Locate every Plasmodium falciparum-infected red blood cell.
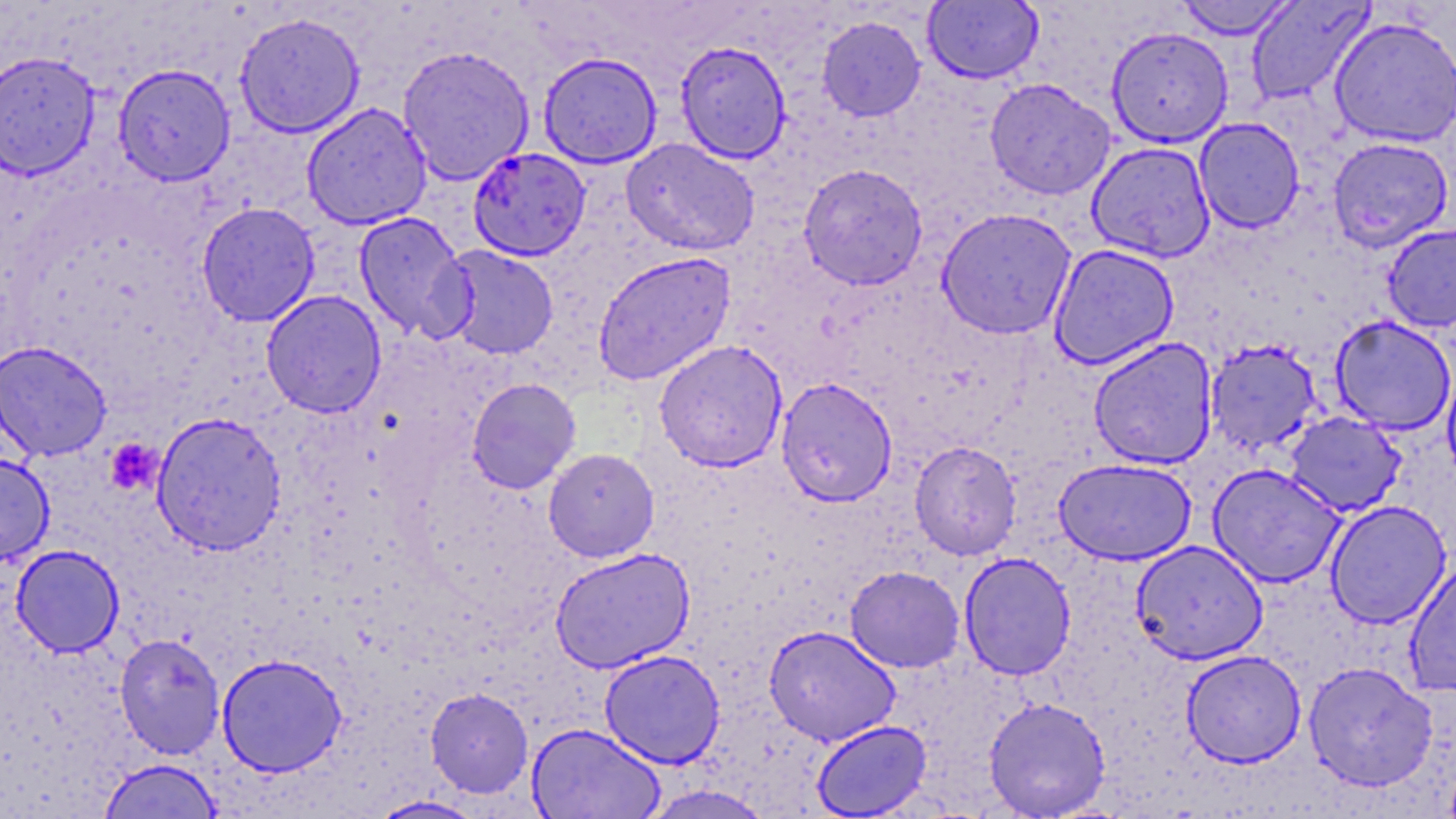

Approximate bounding boxes as [x1, y1, x2, y2] in pixels.
Plasmodium falciparum-infected red blood cells: [468, 147, 591, 261].

slide-level diagnosis = Plasmodium falciparum
field of view = single
image size = 1456×819 pixels
preparation = thin blood smear
magnification = 1000x
modality = light microscopy
stain = May-Grünwald-Giemsa
uninfected red blood cell locations = approximate bounding boxes as [x1, y1, x2, y2] in pixels: [922, 0, 1043, 84], [1175, 0, 1297, 40], [1246, 0, 1375, 105], [233, 11, 366, 139], [816, 15, 926, 122], [1328, 15, 1456, 148], [1106, 27, 1234, 148], [675, 40, 792, 164], [397, 44, 535, 186], [0, 50, 101, 180], [537, 51, 663, 168], [112, 63, 236, 186], [984, 78, 1116, 200], [301, 102, 433, 231], [1193, 117, 1305, 234], [621, 137, 760, 256], [1327, 137, 1454, 252], [1086, 141, 1216, 263], [798, 163, 929, 289], [196, 201, 320, 327], [936, 208, 1077, 339], [353, 212, 474, 342], [1381, 223, 1456, 332], [1048, 243, 1180, 370], [438, 244, 560, 360], [592, 250, 737, 386], [261, 290, 387, 417], [1330, 315, 1456, 435], [1087, 337, 1219, 470], [0, 339, 112, 462], [653, 339, 789, 472], [1205, 339, 1324, 455], [1442, 362, 1456, 484], [775, 377, 898, 507], [466, 378, 581, 494], [1284, 411, 1407, 517], [150, 412, 287, 556], [909, 441, 1022, 560], [542, 448, 659, 562], [0, 454, 55, 564], [1053, 457, 1197, 565], [1208, 464, 1345, 588], [1325, 500, 1452, 629], [1130, 540, 1268, 665], [10, 544, 125, 657], [549, 547, 695, 673], [958, 552, 1076, 680], [1403, 560, 1456, 696], [845, 565, 965, 673], [763, 625, 901, 746], [114, 632, 226, 760], [599, 649, 726, 768], [1181, 649, 1306, 767], [216, 653, 348, 778], [1303, 662, 1438, 792], [425, 687, 534, 798], [983, 696, 1111, 817], [811, 719, 931, 818], [527, 723, 665, 819], [98, 758, 224, 819], [640, 785, 775, 819], [367, 796, 486, 818]
platelet locations = approximate bounding boxes as [x1, y1, x2, y2] in pixels: [105, 438, 162, 495]